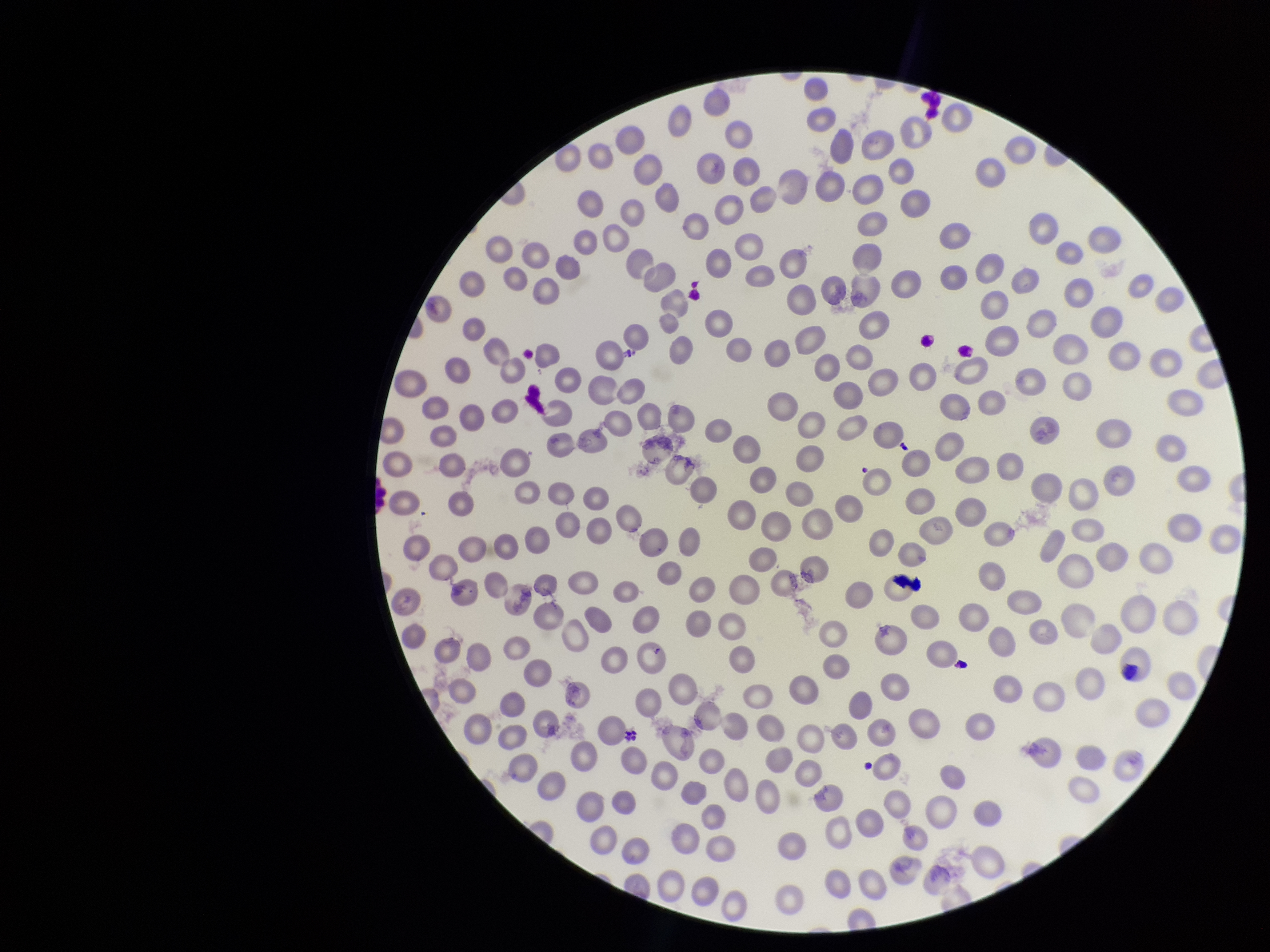

Summary:
  - Image size: 1270×952 pixels
  - Field of view: one from this slide
  - Parasitized red blood cells: none seen
  - Species reported for this patient: Plasmodium vivax
  - Red blood cell count: 263
  - Stain: Giemsa
  - Patient malaria status: infected
  - Capture: smartphone photograph through the microscope eyepiece
  - Parasitized red blood cell count: 0
  - Preparation: thin blood smear